Name the parasite shown.
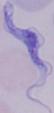
This is a trypanosome.

1000x magnification. Micrograph.